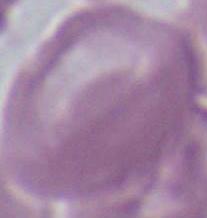

Summary:
  - Modality: photomicrograph
  - Magnification: 1000x
  - Identification: erythrocyte